Report the malaria status of this cell.
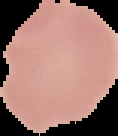

It is uninfected.

Summary:
  - Image size: 118×136 pixels
  - Preparation: thin blood film
  - Image type: cell region segmented out of the field of view; surrounding area masked to black